Locate every blood parasite and identify its species.
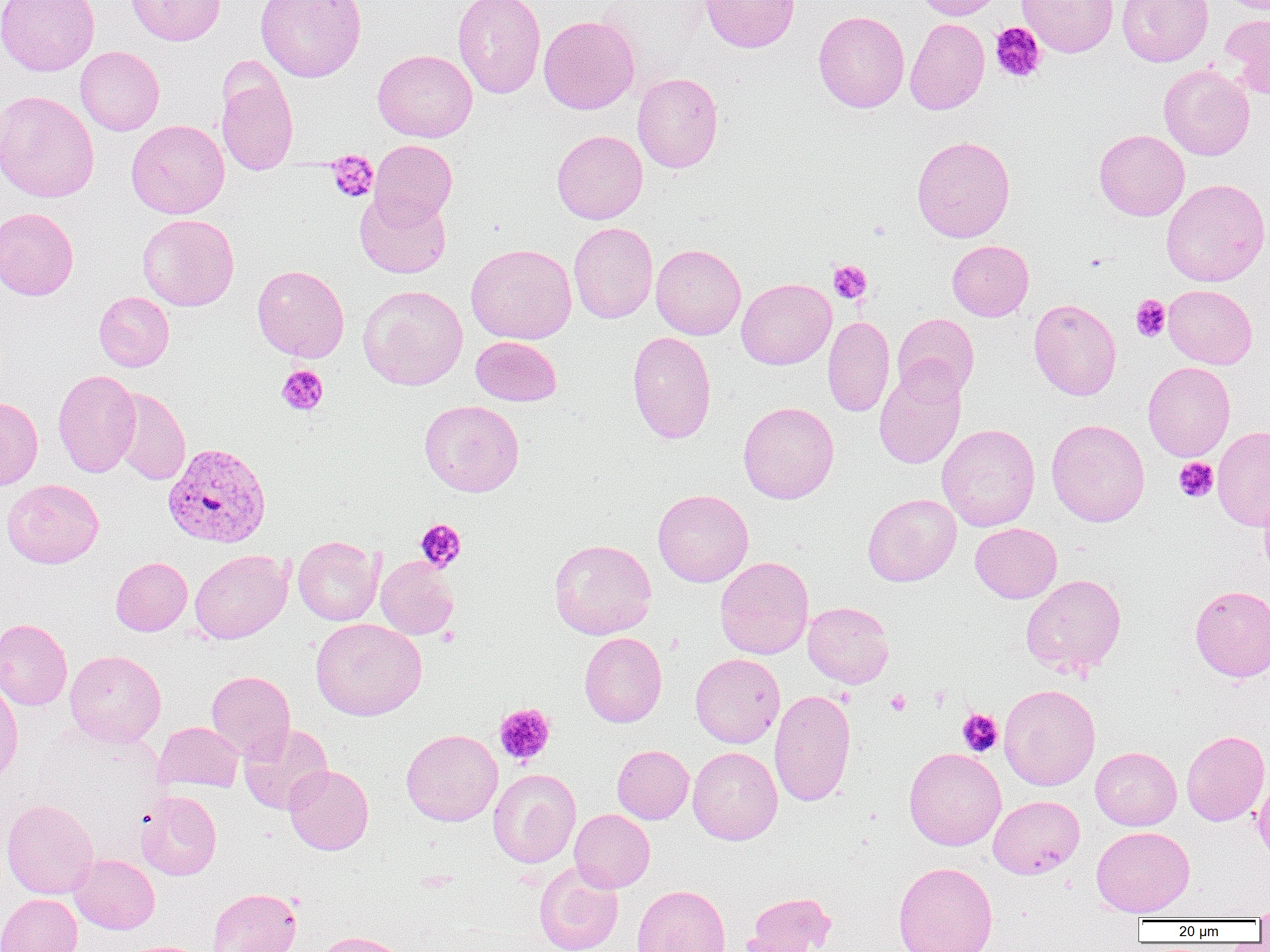
Approximate bounding boxes as (x1,y1)-(x2,y2) corner pairs in pixels.
Plasmodium vivax-infected red blood cells: (163,443)-(271,548).
No Plasmodium falciparum, Plasmodium ovale, Plasmodium malariae, Babesia divergens, or Trypanosoma brucei observed.

Platelet locations: (990,22)-(1046,83), (326,150)-(379,202), (827,260)-(872,304), (1130,295)-(1171,341), (276,364)-(328,416), (1174,458)-(1218,502), (414,518)-(466,573), (928,686)-(950,710), (886,690)-(911,715), (494,703)-(555,767), (957,708)-(1003,757). Uninfected red blood cell locations: (0,0)-(99,76), (126,0)-(225,45), (256,0)-(367,82), (453,0)-(546,99), (699,0)-(800,53), (914,0)-(1002,20), (1017,0)-(1119,57), (1117,0)-(1213,66), (813,11)-(909,112), (1221,13)-(1270,98), (538,15)-(640,114), (905,18)-(990,115), (75,46)-(164,135), (372,49)-(477,142), (216,63)-(299,176), (1158,63)-(1255,160), (632,72)-(724,173), (0,90)-(99,203), (126,119)-(230,219), (1094,129)-(1189,221), (552,130)-(648,224), (912,135)-(1015,243), (369,139)-(457,226), (1161,178)-(1269,287), (355,189)-(452,279), (0,207)-(79,300), (137,214)-(239,311), (568,222)-(658,323), (947,240)-(1034,321), (466,243)-(577,344), (650,244)-(746,339), (252,264)-(349,362), (736,278)-(836,369), (358,284)-(468,390), (1164,284)-(1258,369), (94,292)-(174,371), (1029,298)-(1122,400), (892,313)-(979,401), (823,316)-(895,417), (627,331)-(717,444), (471,336)-(562,406), (1143,361)-(1235,461), (874,364)-(966,470), (52,370)-(141,477), (110,388)-(191,485), (0,396)-(43,491), (419,400)-(524,496), (738,401)-(839,504), (1046,418)-(1150,527), (937,423)-(1040,531), (1212,425)-(1270,531), (2,479)-(103,568), (1258,483)-(1270,578), (653,489)-(753,587), (863,493)-(961,586), (970,523)-(1062,603), (293,535)-(383,625), (549,538)-(657,639), (190,549)-(292,643), (376,556)-(458,639), (715,556)-(814,659), (110,557)-(192,636), (1021,573)-(1127,679), (1190,585)-(1270,682), (803,601)-(894,688), (310,618)-(426,720), (0,619)-(72,710), (579,632)-(667,727), (65,650)-(166,747), (690,653)-(785,748), (206,670)-(295,760), (0,678)-(23,784), (998,684)-(1101,790), (769,688)-(856,807), (154,722)-(243,793), (238,723)-(333,815), (401,729)-(503,826), (1182,730)-(1270,826), (612,745)-(694,824), (688,746)-(783,845), (1091,746)-(1182,830), (904,747)-(1006,850), (284,764)-(374,855), (488,769)-(581,868), (1253,771)-(1269,863), (135,790)-(221,880), (988,795)-(1085,878), (2,799)-(98,900), (570,809)-(655,892), (1091,826)-(1195,917), (70,855)-(159,933), (534,861)-(624,952), (893,861)-(998,952), (631,884)-(730,952), (208,887)-(302,952), (744,892)-(836,952), (0,894)-(83,952), (1254,900)-(1270,927), (312,931)-(412,952). Slide-level diagnosis: Plasmodium vivax. Light microscopy. 1000x magnification. Image is 1270×952 pixels. Thin blood film. Single field of view.